Describe the morphology of the red blood cells.
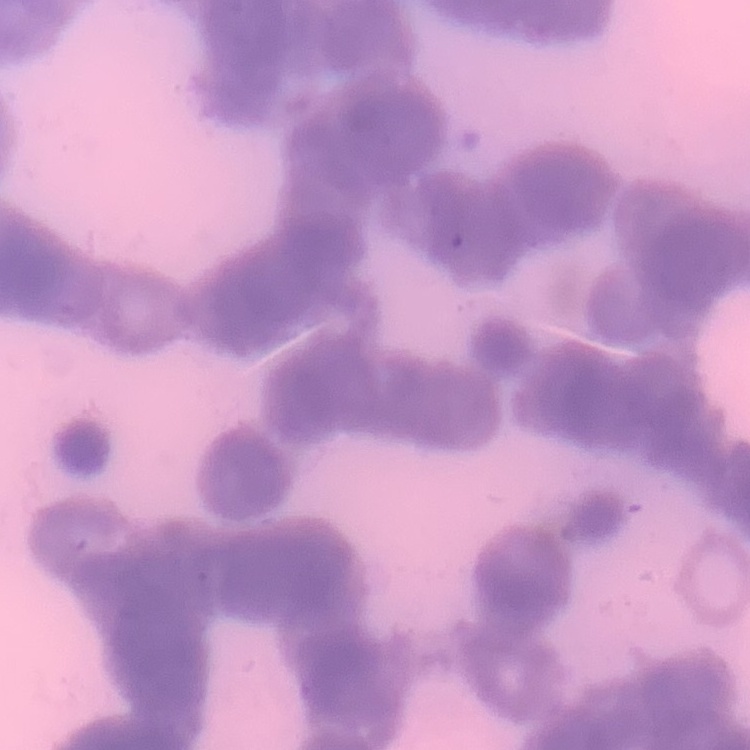

Rouleaux formation.

Field's or Giemsa stain. One tile cut from a larger photomicrograph. Thin peripheral smear.